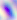

Micrograph. 400x magnification. Toxoplasma gondii is seen.